Identify the blood parasite species.
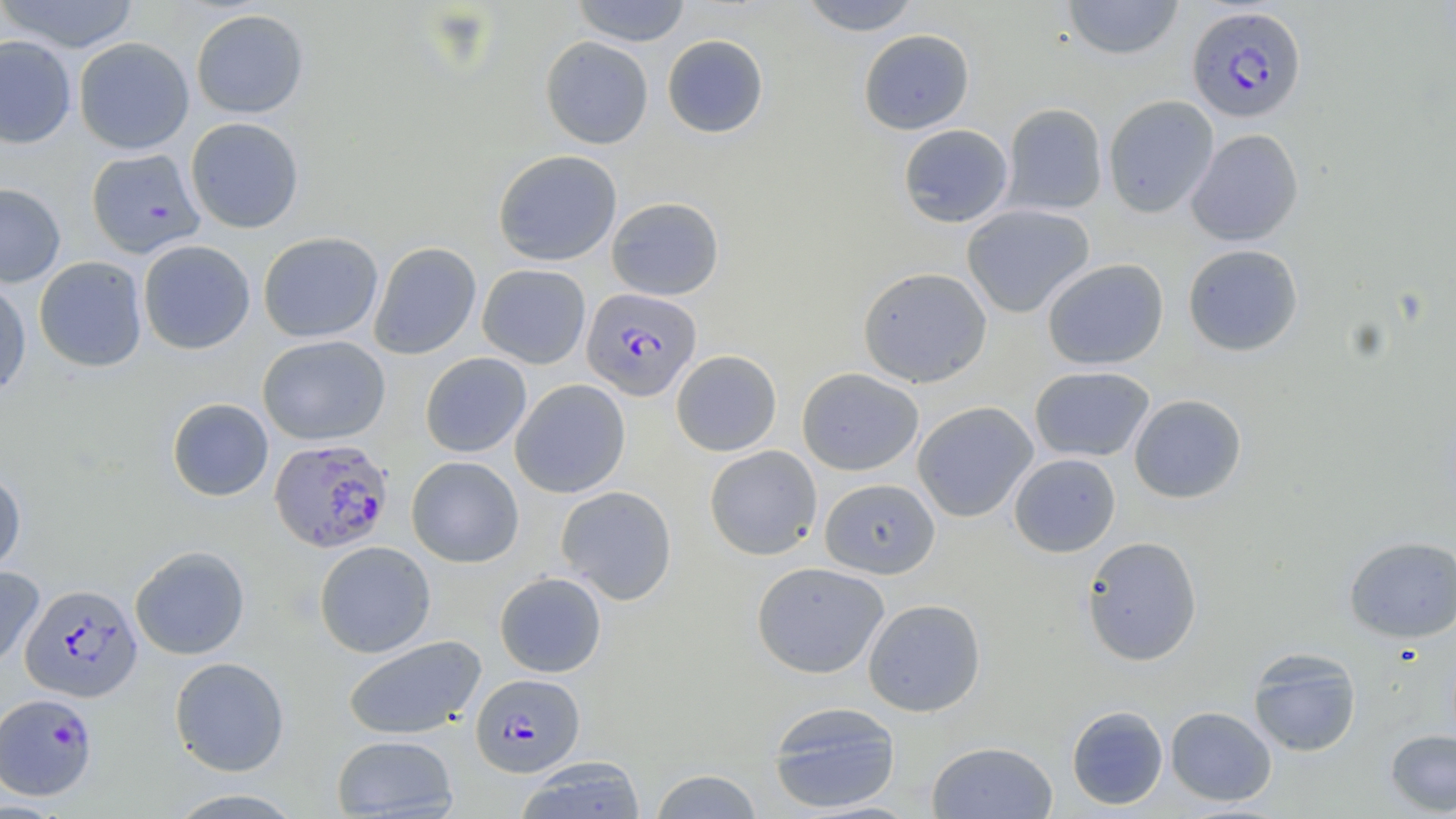
Plasmodium falciparum.

Summary:
  - Coordinate format: approximate bounding boxes as (x1,y1)-(x2,y2) corner pairs in pixels
  - Uninfected red blood cell locations: (0,0)-(140,54), (571,0)-(692,46), (797,0)-(924,36), (1061,0)-(1184,60), (190,8)-(309,119), (858,29)-(975,135), (662,34)-(768,138), (0,35)-(77,148), (540,36)-(654,149), (74,37)-(195,155), (1102,95)-(1219,217), (1001,103)-(1108,215), (185,117)-(304,233), (898,124)-(1014,228), (1186,129)-(1304,246), (85,148)-(206,258), (493,150)-(622,266), (0,182)-(66,288), (606,197)-(724,300), (961,203)-(1095,318), (258,232)-(383,343), (138,239)-(255,354), (369,242)-(482,360), (1182,243)-(1304,357), (34,256)-(147,373), (1042,258)-(1169,370), (477,264)-(591,368), (857,266)-(992,388), (0,277)-(31,397), (257,335)-(391,445), (671,350)-(782,456), (420,352)-(532,458), (1029,366)-(1155,462), (797,367)-(924,476), (510,379)-(631,498), (1129,393)-(1247,504), (167,398)-(273,501), (912,401)-(1039,522), (704,445)-(822,560), (1008,453)-(1121,557), (406,456)-(524,568), (0,469)-(26,577), (819,478)-(941,578), (555,485)-(678,604), (1081,535)-(1202,666), (1344,535)-(1456,643), (314,541)-(436,658), (130,545)-(250,660), (751,561)-(890,679), (0,566)-(45,672), (494,572)-(607,677), (862,598)-(986,716), (342,635)-(487,740), (1247,648)-(1362,757), (169,657)-(290,776), (767,701)-(902,814), (1066,705)-(1168,810), (1165,706)-(1277,806), (1385,729)-(1456,814), (331,734)-(458,819), (926,740)-(1058,818), (514,757)-(646,819), (649,769)-(764,818), (165,788)-(307,818)
  - Plasmodium falciparum-infected red blood cell locations: (1187,6)-(1307,123), (581,287)-(702,400), (269,438)-(393,553), (20,583)-(142,702), (470,673)-(585,777), (0,693)-(97,800)
  - Magnification: 1000x
  - Preparation: thin blood film
  - Modality: optical microscopy
  - Stain: May-Grünwald-Giemsa
  - Field of view: one of a larger specimen
  - Image size: 1456×819 pixels